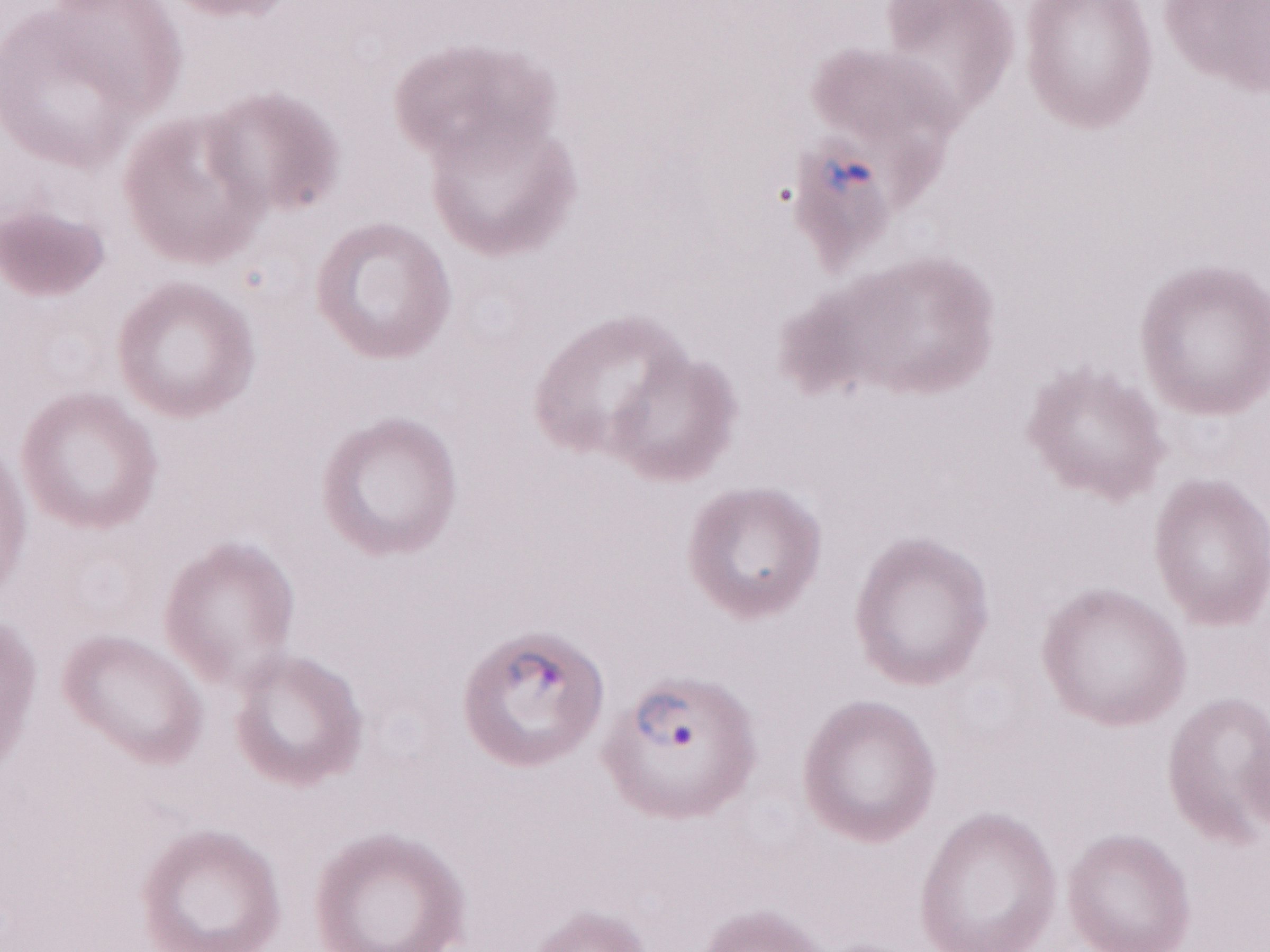
Malaria diagnosis (patient-level): positive. Magnification: 1,000x. Image is 1270×952 pixels. Thin blood smear. Olympus BX43 microscope, Olympus DP73 camera. May-Grünwald-Giemsa (MGG) stain. One field of this slide.